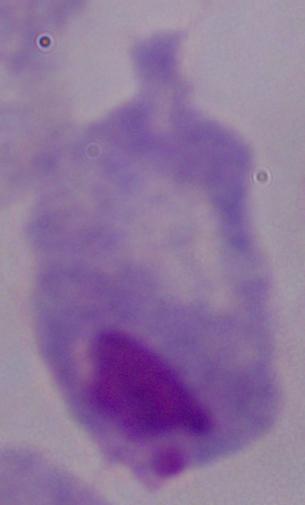

magnification = 1000x
modality = photomicrograph
identification = trichomonad